Report the malaria status of this cell.
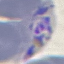

Parasitized.

preparation = thin smear
image type = cell patch, automatically extracted from a larger field of view and resized to 64 × 64 pixels
capture = smartphone through the microscope eyepiece
stain = Giemsa